Classify this cell by malaria status.
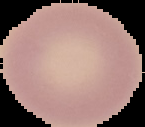
It is uninfected.

Summary:
  - Image size: 145×127 pixels
  - Preparation: thin blood film
  - Image type: segmented cell region on a black background